Point out each Plasmodium parasite.
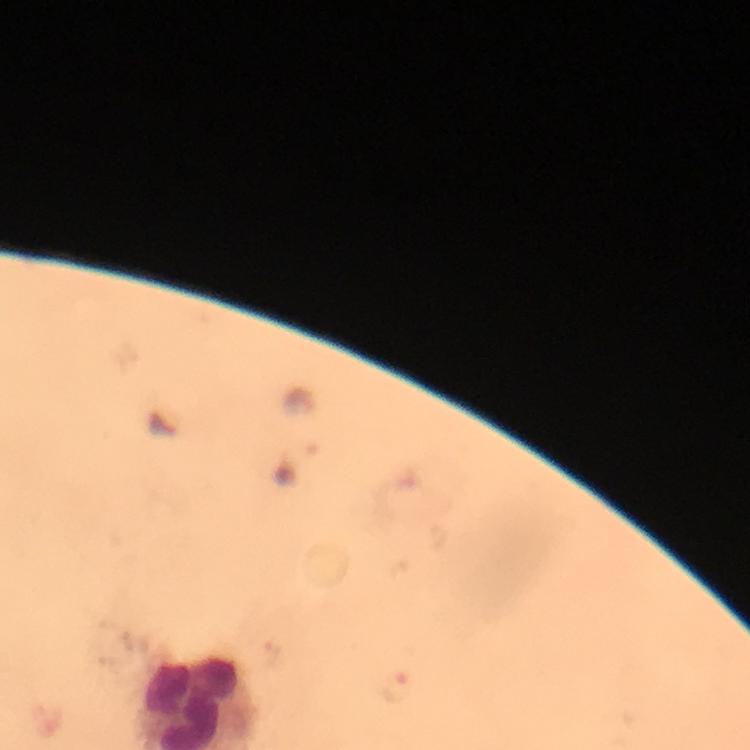
Approximate centers as {x, y} in pixels.
Plasmodium parasites: {396, 689}.

context = from a diagnostic examination for malaria
magnification = 100x
preparation = thick smear
capture = smartphone mounted on the microscope
image size = 750×750 pixels
immersion oil = used
stain = Giemsa
cropped from = one field of view